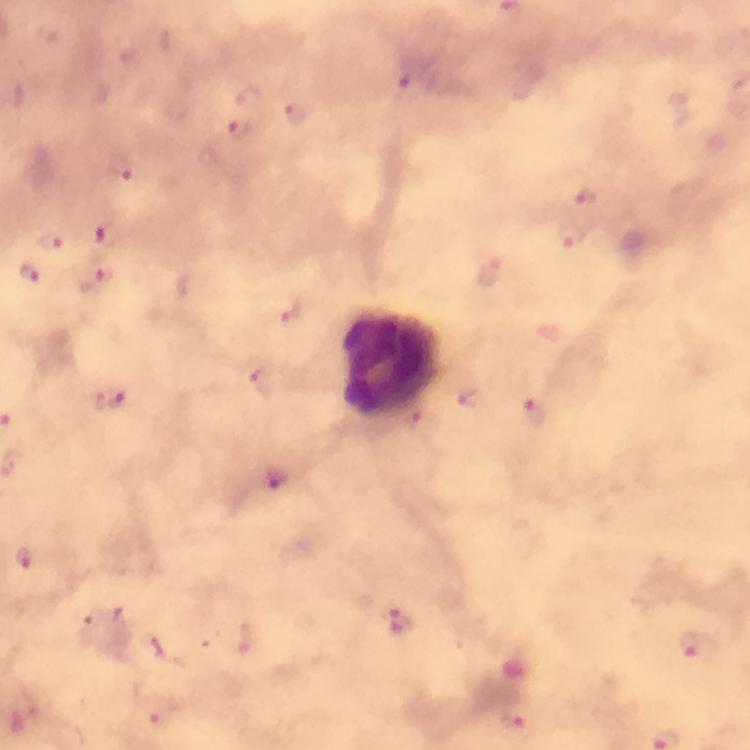

Approximate centers as (x, y) in pixels.
Summary:
  - Leukocyte locations: (388, 362)
  - Plasmodium parasite locations: (408, 83), (246, 97), (296, 113), (240, 131), (120, 170), (585, 199), (107, 234), (573, 238), (49, 242), (492, 272), (29, 274), (96, 282), (287, 311), (261, 382), (113, 397), (535, 415), (419, 421), (696, 648), (515, 724)
  - Image size: 750×750 pixels
  - Cropped from: a single field of view
  - Context: from a diagnostic examination for malaria
  - Immersion oil: used
  - Magnification: 100x
  - Preparation: thick blood film
  - Capture: smartphone camera through the microscope
  - Stain: Giemsa